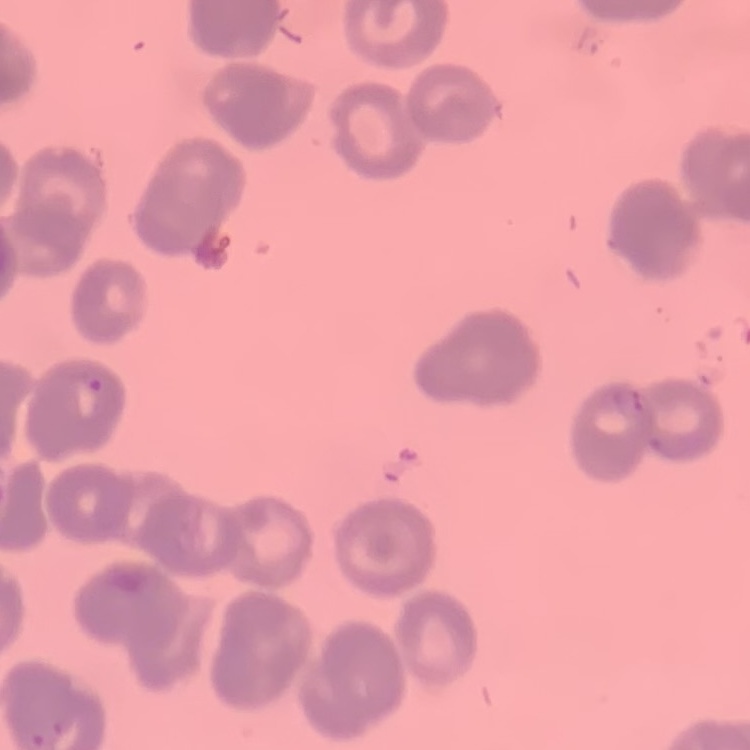

The erythrocytes exhibit rouleaux formation. Thin peripheral smear. Field's or Giemsa stain. One tile cut from a larger photomicrograph.